Identify the blood parasite species.
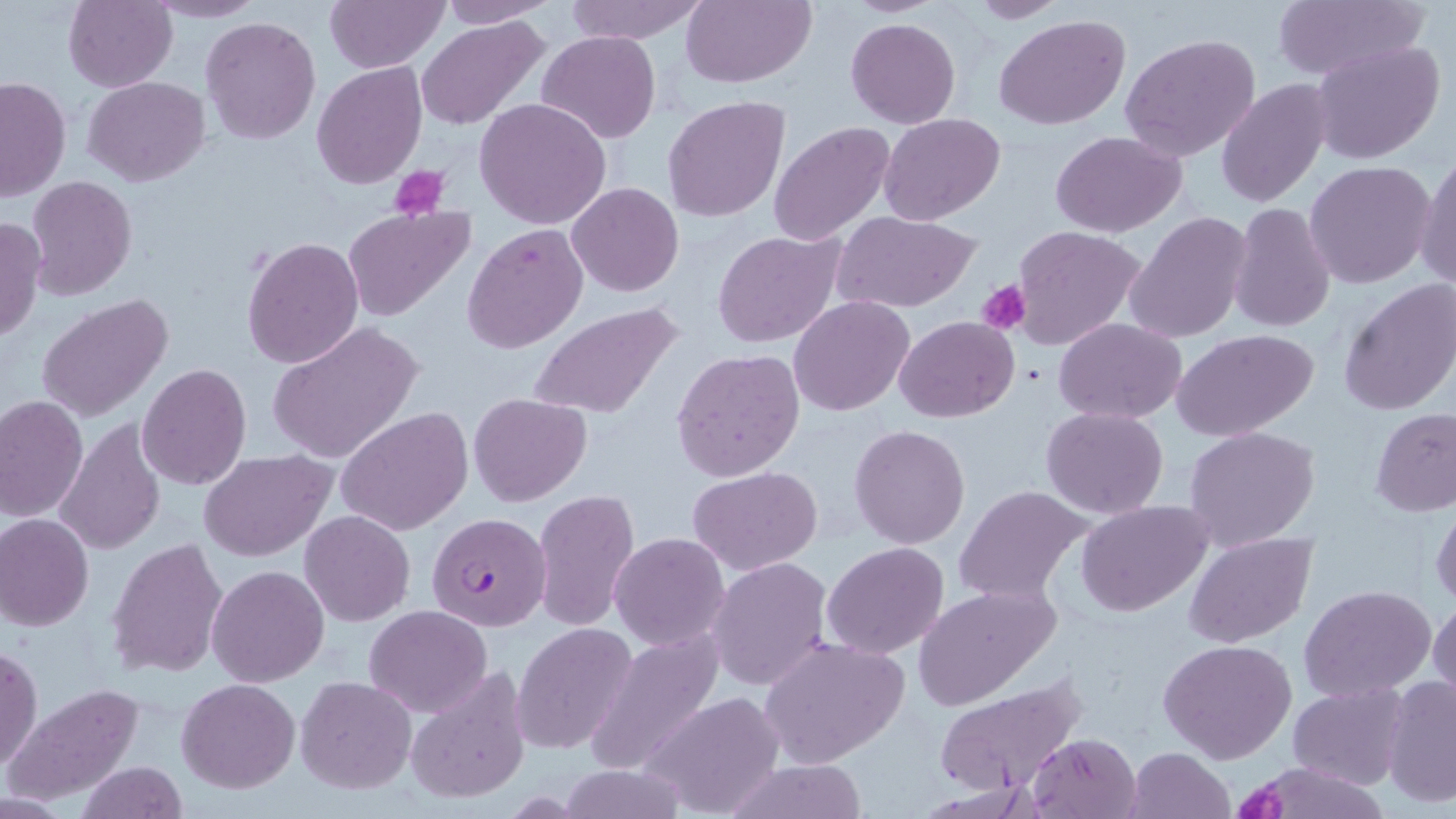

Plasmodium falciparum.

uninfected red blood cell locations = approximate bounding boxes as (x1, y1, x2, y2) in pixels: (64, 0, 177, 91), (564, 0, 708, 43), (680, 0, 816, 89), (958, 0, 1069, 24), (1271, 0, 1426, 81), (145, 1, 268, 23), (326, 1, 446, 72), (439, 1, 558, 25), (994, 15, 1132, 131), (201, 16, 321, 143), (417, 17, 551, 131), (846, 18, 961, 127), (537, 30, 660, 144), (1120, 33, 1260, 161), (1311, 41, 1445, 166), (312, 61, 426, 189), (0, 76, 70, 201), (83, 77, 210, 186), (1218, 78, 1331, 210), (662, 95, 790, 223), (474, 97, 612, 230), (879, 113, 1005, 226), (768, 121, 895, 248), (1050, 131, 1187, 238), (1416, 150, 1456, 292), (1305, 161, 1435, 288), (26, 175, 136, 298), (567, 182, 683, 297), (1229, 202, 1336, 335), (342, 205, 476, 323), (830, 210, 981, 313), (1126, 213, 1254, 344), (0, 216, 45, 341), (462, 224, 587, 355), (1010, 226, 1149, 351), (712, 230, 846, 347), (241, 236, 364, 369), (1338, 278, 1455, 416), (35, 294, 174, 423), (789, 296, 915, 417), (529, 303, 682, 422), (894, 316, 1020, 421), (1054, 318, 1186, 421), (267, 322, 423, 464), (1173, 329, 1319, 442), (671, 349, 805, 481), (136, 363, 251, 489), (469, 393, 592, 505), (0, 396, 87, 520), (338, 406, 473, 537), (1040, 406, 1169, 517), (1371, 406, 1456, 516), (56, 420, 166, 556), (849, 423, 971, 549), (1184, 426, 1319, 550), (198, 450, 334, 561), (688, 467, 823, 573), (952, 485, 1097, 603), (533, 488, 639, 632), (1077, 501, 1214, 616), (1431, 501, 1455, 610), (300, 511, 415, 626), (0, 513, 94, 631), (1184, 532, 1316, 647), (610, 533, 730, 649), (107, 537, 229, 680), (823, 541, 949, 659), (707, 556, 833, 691), (207, 564, 330, 686), (911, 584, 1064, 709), (1300, 584, 1437, 702), (1429, 595, 1456, 712), (365, 605, 492, 716), (511, 622, 637, 755), (756, 636, 909, 769), (1158, 639, 1298, 764), (0, 644, 42, 773), (403, 669, 531, 807), (1381, 674, 1455, 809), (296, 676, 417, 793), (176, 678, 300, 794), (934, 679, 1088, 799), (1288, 682, 1410, 790), (7, 683, 146, 804), (644, 692, 786, 816), (1028, 732, 1143, 818), (1125, 747, 1235, 819), (1239, 759, 1391, 819), (716, 760, 872, 818), (76, 762, 187, 818)
Plasmodium falciparum-infected red blood cell locations = approximate bounding boxes as (x1, y1, x2, y2) in pixels: (427, 511, 549, 631)
stain = May-Grünwald-Giemsa
field of view = single
preparation = thin blood smear
modality = optical microscopy
platelet locations = approximate bounding boxes as (x1, y1, x2, y2) in pixels: (394, 165, 450, 220), (976, 280, 1030, 336), (1241, 780, 1288, 819)
magnification = 1000x
image size = 1456×819 pixels